Report the malaria status.
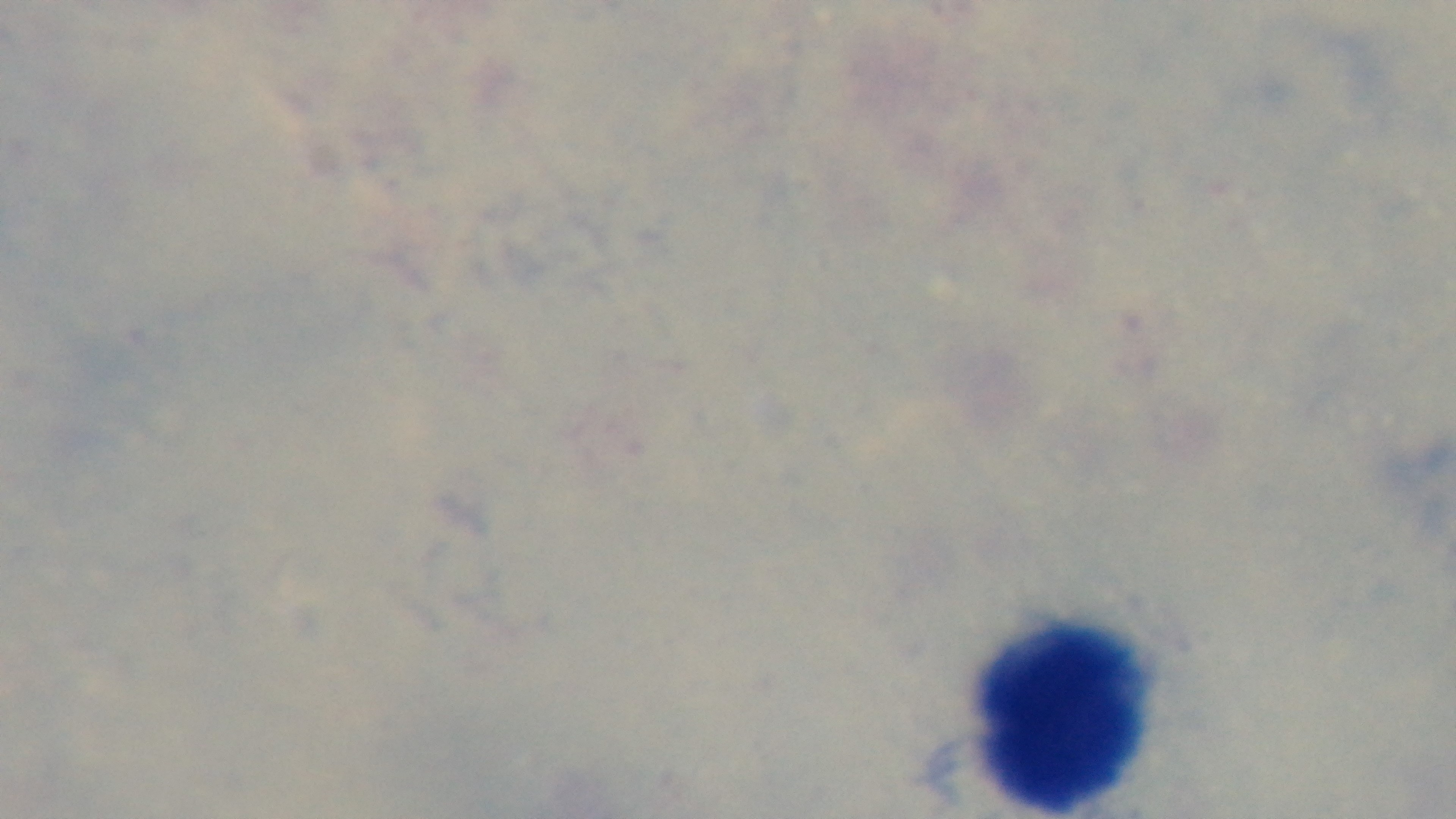
Negative.

objective = 100x oil immersion
modality = light microscopy
field of view = one from the slide
stain = Giemsa
preparation = thick smear
capture = mounted 4K digital camera